Mark where leukocytes are.
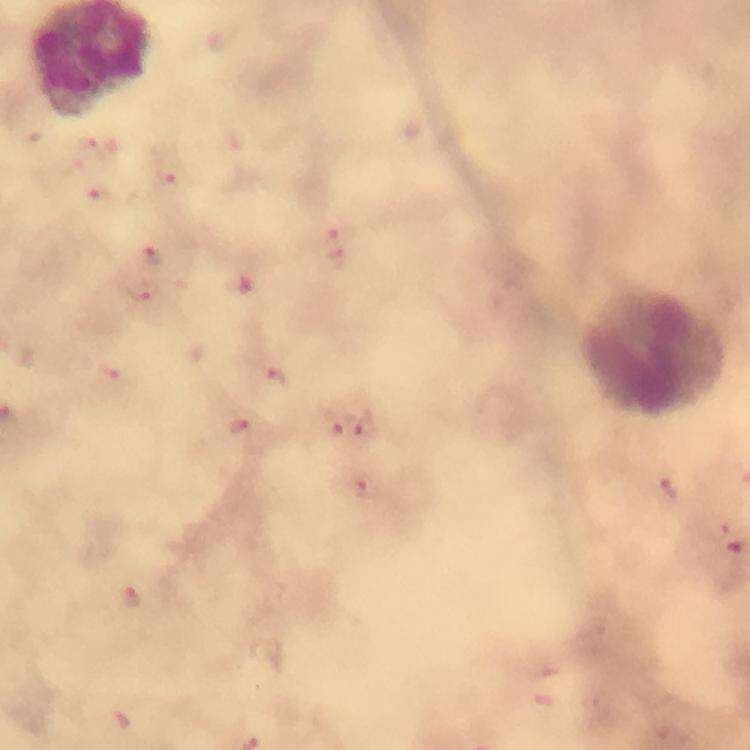
Approximate centers as {x, y} in pixels.
Leukocytes: {651, 351}.

Plasmodium parasite locations: {94, 144}, {174, 173}, {100, 199}, {342, 231}, {153, 255}, {337, 257}, {242, 284}, {144, 292}, {275, 376}, {112, 379}, {336, 423}, {241, 425}, {364, 425}, {668, 486}, {363, 487}, {132, 597}, {124, 722}. Thick blood film. 100x magnification. Image is 750×750 pixels. Cropped region of a single field of view. From a diagnostic examination for malaria. Photographed with a smartphone mounted on the microscope. Immersion oil applied. Giemsa stain.